Locate every Plasmodium ovale-infected red blood cell.
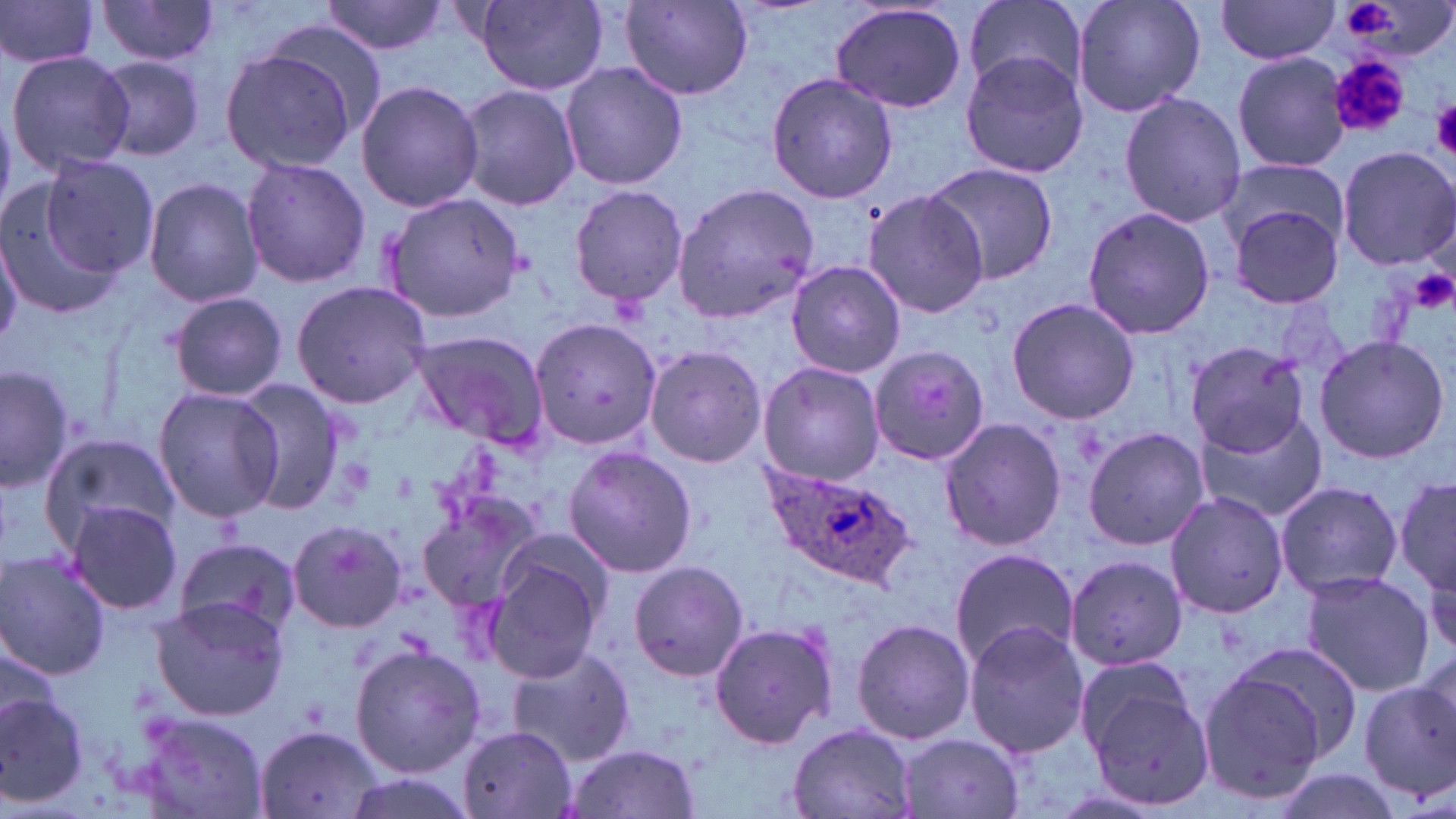
Approximate bounding boxes as named x1/y1/x2/y2 corners in pixels.
Plasmodium ovale-infected red blood cells: (x1=761, y1=463, x2=917, y2=587).

slide_level_diagnosis: Plasmodium ovale
field_of_view: one of a larger specimen
modality: optical microscopy
preparation: thin blood smear
image_size: 1456×819 pixels
uninfected_red_blood_cell_locations: 'approximate bounding boxes as named x1/y1/x2/y2 corners in pixels: (x1=0, y1=0, x2=101, y2=71), (x1=95, y1=0, x2=223, y2=70), (x1=321, y1=0, x2=448, y2=58), (x1=964, y1=0, x2=1085, y2=93), (x1=1071, y1=0, x2=1206, y2=119), (x1=470, y1=1, x2=610, y2=95), (x1=1216, y1=2, x2=1341, y2=63), (x1=619, y1=3, x2=752, y2=99), (x1=830, y1=3, x2=968, y2=116), (x1=217, y1=47, x2=359, y2=174), (x1=5, y1=49, x2=134, y2=174), (x1=958, y1=51, x2=1091, y2=179), (x1=1233, y1=51, x2=1351, y2=173), (x1=94, y1=55, x2=206, y2=163), (x1=559, y1=61, x2=689, y2=191), (x1=765, y1=71, x2=899, y2=204), (x1=355, y1=79, x2=483, y2=213), (x1=456, y1=85, x2=582, y2=211), (x1=1118, y1=91, x2=1245, y2=227), (x1=1335, y1=145, x2=1456, y2=272), (x1=33, y1=153, x2=158, y2=283), (x1=240, y1=157, x2=371, y2=288), (x1=1214, y1=160, x2=1351, y2=255), (x1=922, y1=162, x2=1059, y2=284), (x1=143, y1=176, x2=264, y2=308), (x1=671, y1=180, x2=818, y2=325), (x1=0, y1=183, x2=125, y2=320), (x1=568, y1=184, x2=689, y2=308), (x1=862, y1=188, x2=992, y2=318), (x1=381, y1=191, x2=527, y2=323), (x1=1225, y1=200, x2=1346, y2=310), (x1=1081, y1=206, x2=1215, y2=340), (x1=1, y1=228, x2=23, y2=349), (x1=786, y1=261, x2=907, y2=380), (x1=290, y1=280, x2=433, y2=407), (x1=169, y1=293, x2=291, y2=402), (x1=1006, y1=295, x2=1140, y2=425), (x1=529, y1=314, x2=663, y2=452), (x1=408, y1=330, x2=550, y2=446), (x1=1312, y1=334, x2=1450, y2=465), (x1=1184, y1=338, x2=1311, y2=461), (x1=642, y1=345, x2=768, y2=467), (x1=869, y1=346, x2=991, y2=467), (x1=757, y1=361, x2=884, y2=486), (x1=0, y1=362, x2=75, y2=494), (x1=234, y1=380, x2=355, y2=514), (x1=152, y1=385, x2=285, y2=524), (x1=1195, y1=408, x2=1326, y2=526), (x1=937, y1=417, x2=1065, y2=553), (x1=1082, y1=425, x2=1209, y2=552), (x1=38, y1=431, x2=184, y2=557), (x1=562, y1=446, x2=698, y2=577), (x1=1393, y1=468, x2=1454, y2=605), (x1=1275, y1=481, x2=1403, y2=599), (x1=418, y1=490, x2=546, y2=613), (x1=1164, y1=491, x2=1288, y2=617), (x1=64, y1=500, x2=183, y2=616), (x1=288, y1=519, x2=406, y2=634), (x1=170, y1=541, x2=299, y2=635), (x1=485, y1=546, x2=609, y2=683), (x1=948, y1=547, x2=1080, y2=671), (x1=0, y1=553, x2=113, y2=678), (x1=1064, y1=555, x2=1188, y2=683), (x1=627, y1=560, x2=749, y2=682), (x1=1297, y1=570, x2=1435, y2=698), (x1=148, y1=597, x2=291, y2=721), (x1=851, y1=617, x2=976, y2=747), (x1=708, y1=620, x2=840, y2=751), (x1=963, y1=622, x2=1092, y2=756), (x1=0, y1=640, x2=61, y2=740), (x1=349, y1=642, x2=483, y2=777), (x1=1230, y1=645, x2=1368, y2=770), (x1=507, y1=647, x2=635, y2=766), (x1=1195, y1=663, x2=1336, y2=807), (x1=1082, y1=669, x2=1213, y2=806), (x1=1359, y1=676, x2=1456, y2=806), (x1=0, y1=688, x2=90, y2=810), (x1=134, y1=709, x2=270, y2=815), (x1=787, y1=724, x2=919, y2=819), (x1=255, y1=725, x2=386, y2=818), (x1=455, y1=726, x2=578, y2=819), (x1=896, y1=734, x2=1028, y2=818), (x1=566, y1=744, x2=703, y2=819), (x1=1265, y1=768, x2=1409, y2=819), (x1=346, y1=776, x2=475, y2=819)'
magnification: 1000x
platelet_locations: 'approximate bounding boxes as named x1/y1/x2/y2 corners in pixels: (x1=1339, y1=0, x2=1400, y2=38), (x1=1329, y1=56, x2=1407, y2=137), (x1=1429, y1=100, x2=1456, y2=155), (x1=1409, y1=267, x2=1455, y2=315)'
stain: May-Grünwald-Giemsa